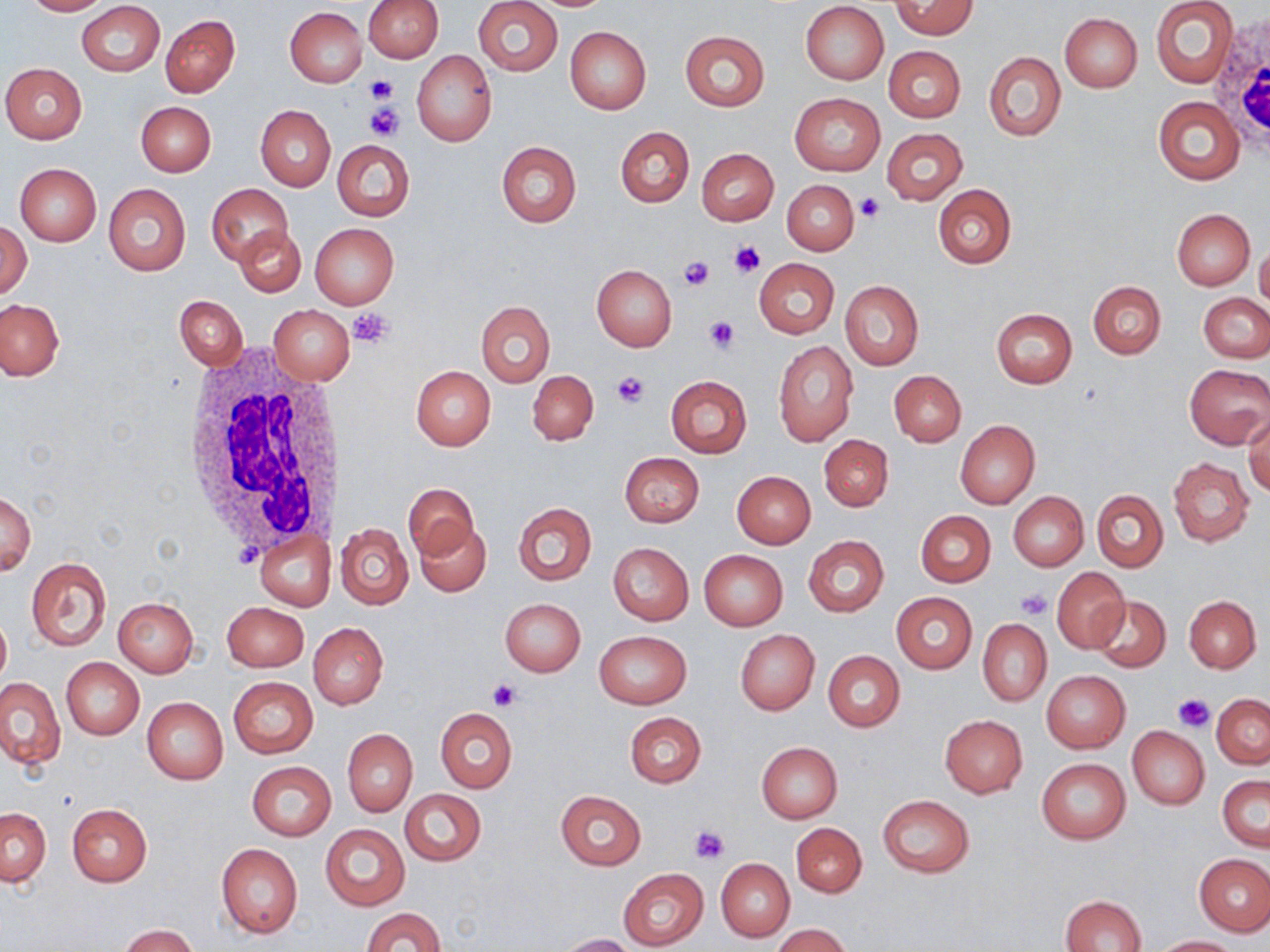

Approximate bounding boxes as [x1, y1, x2, y2] in pixels. Platelet locations: [365, 75, 398, 102], [366, 103, 403, 140], [854, 194, 885, 222], [728, 240, 763, 279], [678, 255, 714, 291], [348, 306, 396, 348], [704, 315, 739, 352], [612, 371, 649, 407], [1017, 589, 1051, 620], [488, 679, 521, 709], [1173, 694, 1213, 733], [689, 826, 729, 864]. Uninfected red blood cell locations: [22, 0, 111, 15], [363, 0, 443, 63], [473, 0, 563, 76], [892, 0, 977, 39], [1151, 0, 1238, 89], [77, 2, 165, 76], [800, 2, 889, 84], [285, 6, 367, 87], [1059, 13, 1141, 92], [160, 14, 240, 97], [565, 25, 651, 115], [680, 30, 769, 110], [884, 46, 965, 123], [412, 50, 497, 147], [983, 51, 1065, 142], [1, 63, 87, 144], [790, 92, 885, 176], [1153, 96, 1245, 185], [136, 101, 216, 176], [255, 105, 335, 191], [615, 126, 694, 207], [882, 128, 967, 205], [332, 140, 415, 220], [496, 141, 581, 228], [696, 147, 778, 225], [14, 163, 101, 246], [782, 179, 859, 255], [103, 183, 190, 276], [207, 183, 293, 265], [933, 185, 1016, 268], [1171, 208, 1254, 289], [1, 222, 31, 300], [310, 222, 399, 309], [236, 226, 306, 297], [1255, 241, 1270, 313], [754, 258, 839, 338], [591, 265, 677, 351], [840, 280, 924, 369], [1087, 281, 1166, 358], [1199, 292, 1270, 363], [175, 295, 247, 372], [0, 299, 63, 381], [477, 301, 554, 387], [268, 304, 355, 384], [992, 308, 1078, 388], [773, 341, 857, 446], [1183, 365, 1269, 449], [410, 366, 495, 451], [527, 370, 598, 446], [889, 371, 965, 446], [666, 375, 752, 456], [1244, 413, 1270, 497], [955, 420, 1040, 508], [819, 435, 894, 511], [620, 452, 704, 528], [1168, 457, 1254, 546], [732, 471, 816, 548], [404, 484, 479, 560], [1093, 490, 1167, 572], [1008, 491, 1089, 571], [1, 492, 36, 576], [513, 502, 597, 584], [916, 510, 995, 587], [415, 520, 492, 596], [336, 523, 414, 609], [255, 530, 335, 610], [803, 536, 889, 616], [608, 542, 694, 625], [699, 550, 788, 630], [25, 557, 112, 651], [1052, 566, 1130, 653], [891, 593, 977, 673], [1091, 595, 1170, 671], [1184, 595, 1261, 672], [499, 597, 585, 677], [114, 598, 198, 675], [222, 601, 309, 671], [0, 612, 11, 689], [979, 618, 1051, 706], [310, 623, 388, 709], [734, 629, 820, 714], [593, 630, 692, 709], [823, 651, 904, 732], [61, 658, 144, 739], [1041, 670, 1130, 753], [0, 677, 64, 769], [228, 677, 317, 758], [1211, 694, 1270, 767], [142, 697, 228, 784], [435, 708, 517, 793], [624, 713, 706, 788], [939, 715, 1027, 798], [1127, 726, 1209, 808], [343, 729, 417, 816], [756, 742, 842, 823], [1036, 758, 1131, 844], [248, 761, 335, 841], [1218, 776, 1269, 852], [401, 790, 486, 865], [556, 790, 646, 869], [878, 794, 974, 877], [67, 804, 152, 886], [1, 807, 51, 887], [792, 822, 866, 897], [320, 824, 409, 911], [217, 842, 303, 939], [1195, 853, 1270, 936], [717, 859, 794, 941], [618, 868, 709, 950], [1060, 894, 1147, 951], [363, 907, 444, 952], [118, 924, 199, 952], [774, 924, 850, 952], [559, 933, 635, 952], [1152, 935, 1242, 951]. White blood cell locations: [1212, 15, 1270, 149], [182, 353, 346, 549]. Slide-level diagnosis: negative for blood parasites. Image is 1270×952 pixels. Optical microscopy. One field of a larger specimen. 1000x magnification. May-Grünwald-Giemsa-stained preparation. Thin blood film.